Classify this cell by malaria status.
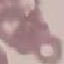

Uninfected.

Giemsa stain. Cell patch, automatically extracted from a larger field of view and resized to 64 × 64 pixels. Thin blood film. Photographed with a smartphone camera at the microscope eyepiece.